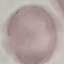

Summary:
  - Result: no malaria parasites seen
  - Capture: smartphone through the microscope eyepiece
  - Preparation: thin smear
  - Stain: Giemsa
  - Image type: cell patch, automatically extracted from a larger field of view and resized to 64 × 64 pixels